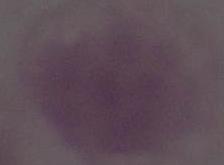 Micrograph. 1000x magnification. A red blood cell is seen.